Report the malaria status of this cell.
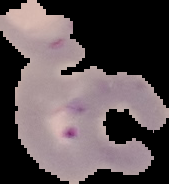
Parasitized.

The area outside the segmented cell region is set to black. Image is 169×184 pixels. From a thin blood film.